Identify the blood parasite species.
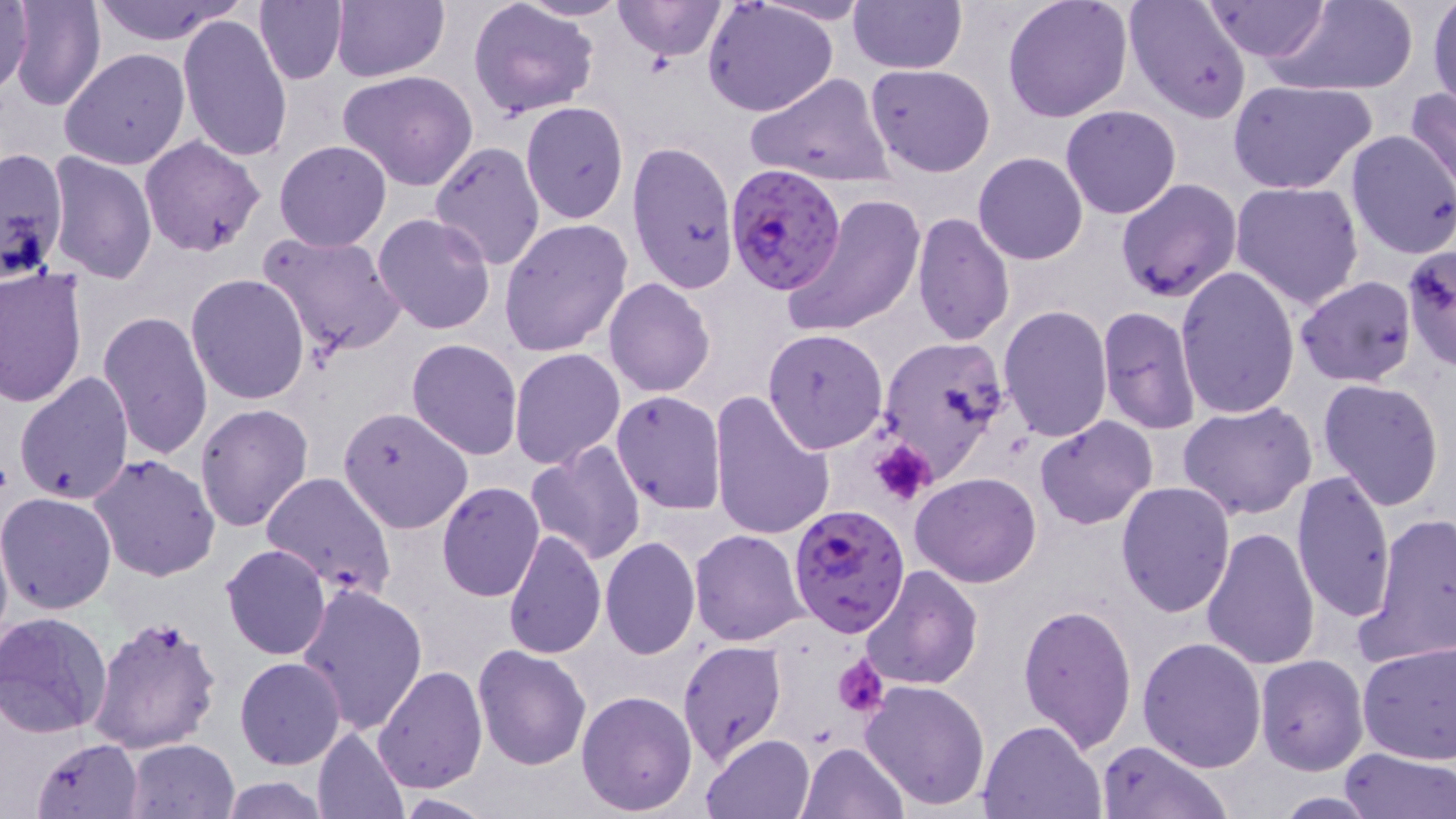
Plasmodium falciparum.

modality = light microscopy
preparation = thin blood film
stain = May-Grünwald-Giemsa
platelet locations = approximate bounding boxes as (x1, y1, x2, y2) in pixels: (867, 436, 937, 506), (833, 654, 888, 717)
Plasmodium falciparum-infected red blood cell locations = approximate bounding boxes as (x1, y1, x2, y2) in pixels: (723, 164, 847, 294), (787, 504, 909, 638)
magnification = 1000x
image size = 1456×819 pixels
field of view = single
uninfected red blood cell locations = approximate bounding boxes as (x1, y1, x2, y2) in pixels: (0, 0, 34, 98), (8, 0, 106, 112), (92, 0, 245, 47), (253, 0, 348, 85), (331, 0, 449, 82), (514, 0, 633, 21), (612, 0, 729, 60), (847, 0, 966, 73), (1003, 0, 1132, 121), (1124, 0, 1254, 124), (1265, 0, 1420, 95), (1427, 0, 1456, 110), (468, 1, 597, 119), (704, 1, 839, 116), (757, 2, 874, 25), (1198, 2, 1332, 63), (177, 14, 293, 163), (60, 48, 189, 170), (864, 63, 996, 176), (337, 71, 480, 190), (745, 72, 894, 188), (1228, 79, 1376, 195), (1405, 87, 1456, 202), (521, 102, 630, 223), (1061, 104, 1182, 219), (1345, 130, 1456, 258), (139, 135, 266, 256), (274, 139, 392, 252), (429, 142, 546, 271), (628, 142, 736, 293), (0, 145, 69, 283), (45, 152, 157, 284), (973, 152, 1088, 264), (933, 177, 1054, 317), (1115, 178, 1240, 302), (1231, 180, 1365, 308), (781, 193, 925, 337), (911, 213, 1015, 346), (371, 214, 496, 335), (500, 217, 633, 358), (258, 229, 408, 360), (1403, 246, 1456, 369), (0, 264, 87, 406), (1174, 266, 1301, 421), (186, 274, 311, 406), (1295, 275, 1419, 387), (604, 278, 715, 399), (999, 304, 1111, 442), (1097, 306, 1200, 434), (99, 310, 213, 459), (761, 328, 887, 453), (876, 336, 1014, 486), (407, 338, 523, 460), (509, 348, 625, 469), (14, 370, 135, 507), (1317, 377, 1446, 511), (610, 390, 726, 514), (710, 391, 835, 542), (1178, 400, 1318, 519), (194, 403, 315, 533), (337, 405, 474, 535), (1035, 416, 1158, 531), (526, 441, 646, 566), (87, 453, 221, 582), (1289, 470, 1395, 622), (261, 471, 396, 598), (910, 473, 1041, 587), (1115, 481, 1236, 617), (436, 482, 546, 601), (0, 491, 117, 614), (1368, 511, 1456, 665), (0, 521, 13, 654), (1202, 526, 1320, 671), (502, 529, 606, 660), (689, 530, 809, 646), (600, 537, 700, 659), (220, 544, 332, 660), (858, 565, 983, 692), (296, 583, 428, 734), (1017, 603, 1138, 753), (0, 612, 114, 739), (89, 615, 222, 758), (1136, 636, 1268, 773), (678, 639, 788, 765), (1357, 642, 1456, 764), (472, 643, 593, 770), (1257, 654, 1369, 775), (235, 658, 345, 770), (373, 664, 487, 792), (859, 678, 991, 811), (576, 690, 698, 816), (977, 719, 1107, 818), (313, 725, 411, 819), (702, 732, 815, 819), (31, 738, 143, 819), (124, 738, 240, 819), (1096, 740, 1229, 819), (796, 742, 907, 819), (1338, 746, 1453, 819), (217, 776, 332, 818), (1269, 792, 1386, 817), (392, 794, 493, 817)